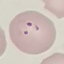

malaria status = parasitized
image type = automatically extracted cell patch, resized to 64 × 64 pixels
preparation = thin blood film
capture = smartphone camera at the microscope eyepiece
stain = Giemsa